Assess this cell for malaria.
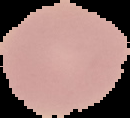
It is uninfected.

image size = 130×118 pixels
preparation = thin blood film
image type = segmented cell region on a black background